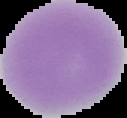

From a thin blood film. Segmented cell region on a black background. Image is 127×118 pixels. Malaria status: uninfected.